Name the parasite shown.
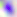
Toxoplasma gondii.

Photomicrograph. Captured at 400x magnification.